Point out every Plasmodium parasite.
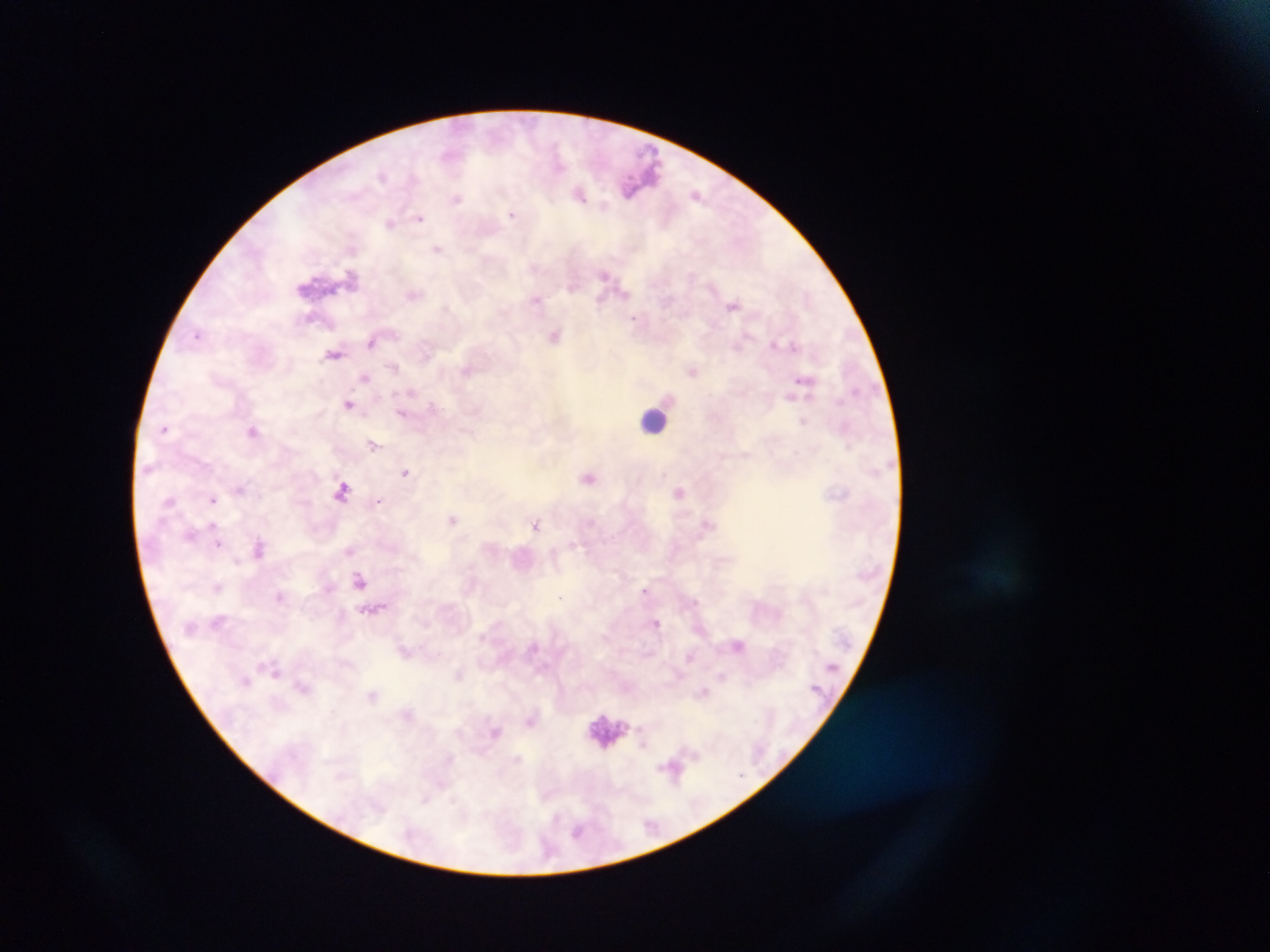

Approximate centers as x y in pixels.
Plasmodium parasites: 382 176; 579 193; 696 193; 457 198; 604 206; 512 214; 420 217; 390 223; 437 249; 604 274; 351 276; 625 293; 413 295; 536 299; 600 302; 732 305; 634 318; 198 335; 555 336; 371 342; 775 345; 794 345; 335 354; 393 367; 467 370; 693 371; 365 377; 802 380; 411 393; 790 396; 348 404; 431 404; 401 413; 803 422; 166 427; 253 431; 373 445; 405 472; 589 478; 240 489; 342 491; 680 493; 213 500; 170 501; 379 501; 453 519; 536 524; 191 535; 219 543; 573 545; 259 547; 349 550; 237 560; 359 580; 217 588; 644 590; 279 596; 561 597; 695 601; 657 622; 739 645; 276 672; 458 674; 722 676; 246 681; 704 693; 372 695; 531 720; 496 732; 643 743; 425 799; 578 831.

Leukocyte locations: 654 420; 605 728. Sample from Ghana. Thick blood film. Image is 1270×952 pixels. Mobile-phone photograph taken through the microscope. One field of view.